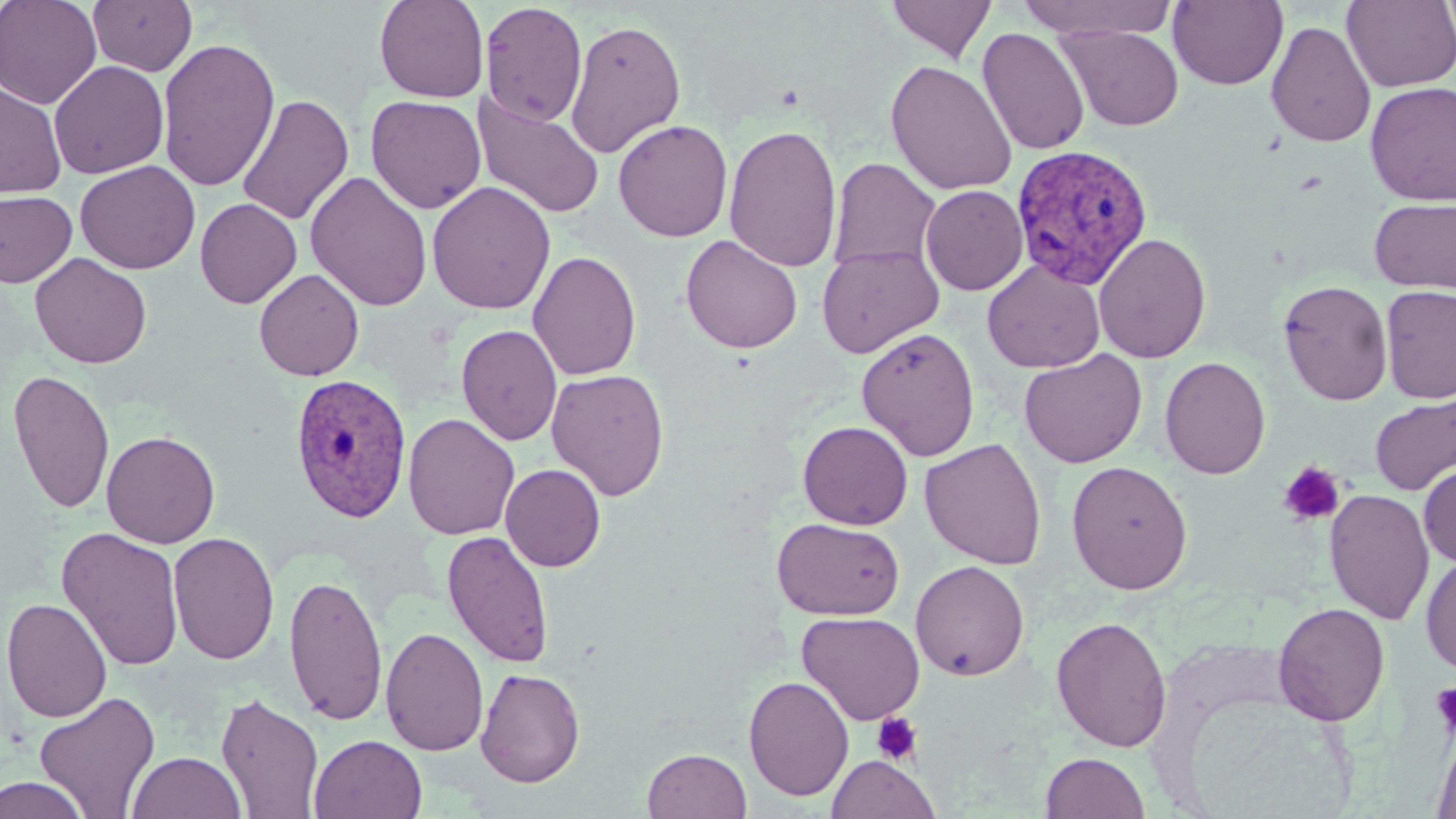

Approximate bounding boxes as named x1/y1/x2/y2 corners in pixels. Plasmodium vivax-infected red blood cell locations: (x1=1010, y1=143, x2=1153, y2=290), (x1=289, y1=372, x2=414, y2=523). Platelet locations: (x1=1279, y1=461, x2=1345, y2=525), (x1=1430, y1=682, x2=1456, y2=739), (x1=871, y1=712, x2=924, y2=765). Uninfected red blood cell locations: (x1=0, y1=0, x2=102, y2=110), (x1=88, y1=0, x2=198, y2=76), (x1=374, y1=0, x2=489, y2=103), (x1=886, y1=0, x2=996, y2=63), (x1=1016, y1=0, x2=1178, y2=40), (x1=1168, y1=0, x2=1288, y2=90), (x1=1342, y1=1, x2=1456, y2=92), (x1=479, y1=2, x2=587, y2=126), (x1=565, y1=19, x2=686, y2=157), (x1=1266, y1=20, x2=1376, y2=148), (x1=1058, y1=25, x2=1184, y2=131), (x1=977, y1=27, x2=1089, y2=156), (x1=157, y1=37, x2=280, y2=192), (x1=49, y1=60, x2=169, y2=179), (x1=885, y1=60, x2=1017, y2=196), (x1=0, y1=82, x2=66, y2=198), (x1=1364, y1=82, x2=1456, y2=205), (x1=472, y1=91, x2=605, y2=219), (x1=236, y1=94, x2=353, y2=225), (x1=366, y1=95, x2=486, y2=213), (x1=612, y1=119, x2=733, y2=242), (x1=724, y1=122, x2=842, y2=272), (x1=829, y1=158, x2=941, y2=274), (x1=75, y1=160, x2=200, y2=274), (x1=305, y1=171, x2=433, y2=312), (x1=427, y1=181, x2=556, y2=315), (x1=921, y1=185, x2=1028, y2=295), (x1=1, y1=190, x2=77, y2=288), (x1=1370, y1=197, x2=1456, y2=294), (x1=195, y1=198, x2=302, y2=309), (x1=1094, y1=232, x2=1212, y2=364), (x1=680, y1=235, x2=803, y2=353), (x1=817, y1=244, x2=943, y2=358), (x1=527, y1=250, x2=642, y2=381), (x1=30, y1=253, x2=152, y2=369), (x1=983, y1=261, x2=1104, y2=373), (x1=254, y1=269, x2=364, y2=381), (x1=1278, y1=279, x2=1393, y2=405), (x1=1379, y1=285, x2=1456, y2=404), (x1=456, y1=324, x2=562, y2=446), (x1=856, y1=327, x2=980, y2=461), (x1=1019, y1=349, x2=1147, y2=468), (x1=1160, y1=356, x2=1271, y2=480), (x1=546, y1=368, x2=669, y2=501), (x1=8, y1=369, x2=115, y2=515), (x1=1370, y1=392, x2=1456, y2=497), (x1=403, y1=413, x2=520, y2=540), (x1=797, y1=421, x2=913, y2=530), (x1=101, y1=430, x2=220, y2=548), (x1=920, y1=438, x2=1046, y2=569), (x1=1066, y1=460, x2=1193, y2=595), (x1=1419, y1=462, x2=1456, y2=566), (x1=500, y1=464, x2=606, y2=571), (x1=1324, y1=489, x2=1435, y2=625), (x1=771, y1=517, x2=905, y2=620), (x1=57, y1=527, x2=185, y2=671), (x1=442, y1=530, x2=554, y2=668), (x1=168, y1=531, x2=279, y2=665), (x1=1420, y1=554, x2=1456, y2=675), (x1=911, y1=560, x2=1030, y2=681), (x1=283, y1=573, x2=387, y2=725), (x1=2, y1=597, x2=113, y2=723), (x1=1272, y1=602, x2=1390, y2=727), (x1=796, y1=611, x2=924, y2=725), (x1=1050, y1=615, x2=1173, y2=752), (x1=381, y1=627, x2=488, y2=756), (x1=475, y1=667, x2=585, y2=788), (x1=743, y1=675, x2=854, y2=801), (x1=34, y1=690, x2=161, y2=819), (x1=216, y1=692, x2=324, y2=819), (x1=1172, y1=692, x2=1362, y2=819), (x1=1431, y1=725, x2=1456, y2=819), (x1=309, y1=733, x2=427, y2=819), (x1=642, y1=748, x2=751, y2=819), (x1=127, y1=751, x2=246, y2=818), (x1=1040, y1=751, x2=1150, y2=818), (x1=826, y1=754, x2=941, y2=819), (x1=0, y1=775, x2=90, y2=819). Slide-level diagnosis: Plasmodium vivax. Captured at 1000x magnification. Single field of view. Thin blood smear. May-Grünwald-Giemsa-stained preparation. Optical microscopy. Image is 1456×819 pixels.